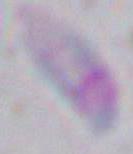
{
  "identification": "Toxoplasma gondii",
  "magnification": "1000x",
  "modality": "photomicrograph"
}